Outline each Plasmodium ovale-infected red blood cell.
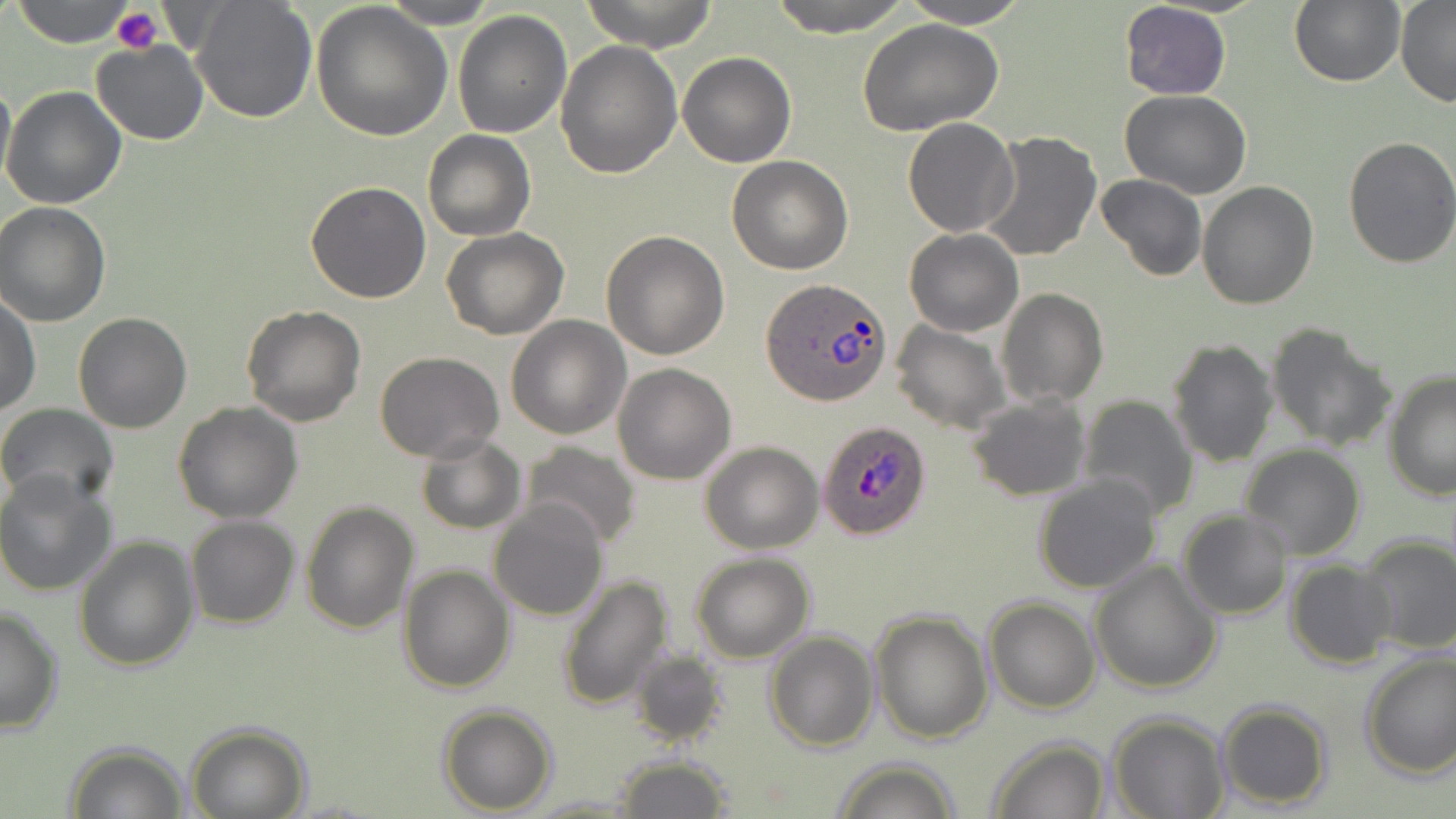

Approximate bounding boxes as (x1,y1)-(x2,y2) corner pairs in pixels.
Plasmodium ovale-infected red blood cells: (762,278)-(891,407), (816,421)-(931,541).

Summary:
  - Uninfected red blood cell locations: (13,0)-(134,47), (382,0)-(497,27), (580,0)-(720,51), (765,0)-(913,37), (899,0)-(1029,27), (1290,0)-(1405,87), (1396,0)-(1456,106), (191,1)-(318,124), (312,1)-(450,140), (1120,2)-(1233,101), (452,9)-(573,138), (856,19)-(1004,136), (555,40)-(682,178), (90,42)-(210,146), (678,52)-(795,167), (0,77)-(14,194), (2,84)-(128,209), (1120,89)-(1251,200), (902,118)-(1018,236), (422,129)-(536,242), (979,131)-(1101,262), (1341,136)-(1456,269), (727,156)-(853,274), (1095,175)-(1207,280), (305,180)-(431,303), (1197,182)-(1319,310), (0,202)-(110,326), (441,228)-(569,340), (905,228)-(1023,338), (601,230)-(730,359), (996,287)-(1108,407), (1,291)-(41,417), (242,305)-(366,427), (73,312)-(192,433), (506,316)-(632,440), (890,320)-(1009,434), (1264,322)-(1395,453), (1166,337)-(1279,468), (375,351)-(504,462), (612,362)-(738,484), (1382,370)-(1456,501), (966,393)-(1093,501), (1077,395)-(1200,521), (173,401)-(303,524), (0,402)-(121,510), (415,436)-(526,534), (699,440)-(823,553), (517,442)-(642,550), (1239,446)-(1367,560), (0,473)-(121,599), (1032,474)-(1163,592), (489,499)-(610,621), (299,500)-(419,635), (1177,511)-(1291,620), (186,516)-(299,629), (1358,534)-(1456,654), (74,537)-(199,671), (690,552)-(815,661), (1089,559)-(1222,694), (1286,559)-(1396,670), (398,564)-(516,693), (556,573)-(676,709), (983,599)-(1100,713), (0,604)-(62,736), (870,609)-(994,743), (764,631)-(879,750), (1357,649)-(1456,779), (629,651)-(730,748), (1215,700)-(1333,811), (438,704)-(557,814), (1108,713)-(1229,819), (185,722)-(311,818), (987,735)-(1111,818), (65,742)-(190,819), (612,755)-(733,819), (828,758)-(962,819), (526,793)-(640,817)
  - Platelet locations: (111,7)-(163,55)
  - Slide-level diagnosis: Plasmodium ovale
  - Stain: May-Grünwald-Giemsa
  - Field of view: single
  - Modality: optical microscopy
  - Preparation: thin blood smear
  - Image size: 1456×819 pixels
  - Magnification: 1000x